Assess the morphology of the erythrocytes.
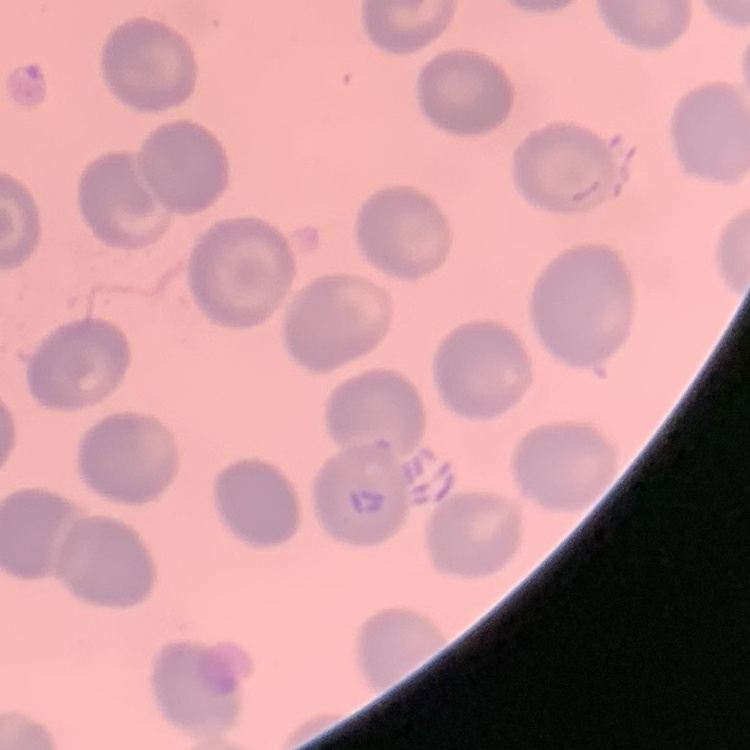

No rouleaux formation.

One tile cut from a larger photomicrograph. Thin peripheral smear. Stained with either Field's or Giemsa.